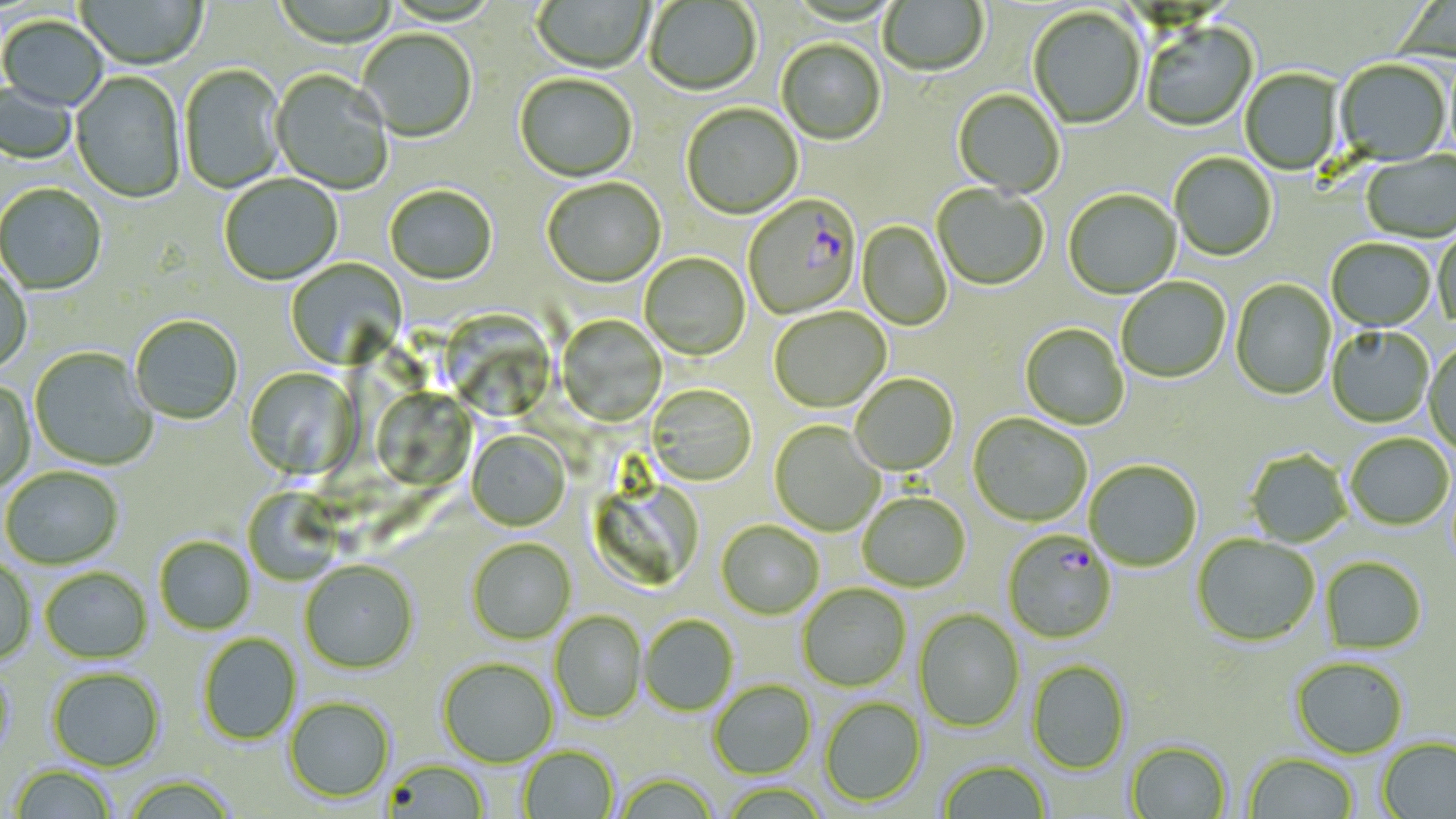

Summary:
  - Coordinate format: approximate bounding boxes as named x1/y1/x2/y2 corners in pixels
  - Uninfected red blood cell locations: (x1=272, y1=0, x2=399, y2=50), (x1=531, y1=0, x2=654, y2=75), (x1=879, y1=0, x2=988, y2=78), (x1=75, y1=1, x2=207, y2=72), (x1=644, y1=1, x2=761, y2=97), (x1=1028, y1=8, x2=1146, y2=130), (x1=0, y1=17, x2=108, y2=113), (x1=1141, y1=23, x2=1259, y2=133), (x1=356, y1=30, x2=477, y2=144), (x1=777, y1=41, x2=886, y2=146), (x1=1334, y1=61, x2=1451, y2=166), (x1=179, y1=65, x2=288, y2=195), (x1=1240, y1=69, x2=1344, y2=176), (x1=270, y1=71, x2=393, y2=195), (x1=70, y1=73, x2=186, y2=204), (x1=515, y1=76, x2=638, y2=183), (x1=0, y1=81, x2=77, y2=166), (x1=953, y1=90, x2=1065, y2=199), (x1=681, y1=104, x2=803, y2=220), (x1=1362, y1=152, x2=1456, y2=244), (x1=1169, y1=154, x2=1277, y2=262), (x1=220, y1=175, x2=343, y2=287), (x1=543, y1=179, x2=666, y2=290), (x1=0, y1=185, x2=107, y2=296), (x1=932, y1=185, x2=1049, y2=291), (x1=384, y1=187, x2=498, y2=287), (x1=1064, y1=190, x2=1181, y2=299), (x1=858, y1=221, x2=952, y2=332), (x1=1434, y1=229, x2=1456, y2=331), (x1=1326, y1=239, x2=1436, y2=333), (x1=639, y1=253, x2=751, y2=361), (x1=285, y1=257, x2=408, y2=370), (x1=0, y1=265, x2=32, y2=375), (x1=1116, y1=278, x2=1231, y2=383), (x1=1230, y1=279, x2=1336, y2=400), (x1=770, y1=308, x2=892, y2=413), (x1=436, y1=309, x2=559, y2=423), (x1=130, y1=315, x2=243, y2=425), (x1=557, y1=315, x2=666, y2=427), (x1=1020, y1=324, x2=1130, y2=430), (x1=1327, y1=327, x2=1434, y2=428), (x1=1424, y1=342, x2=1456, y2=455), (x1=30, y1=348, x2=157, y2=471), (x1=243, y1=367, x2=361, y2=481), (x1=851, y1=374, x2=959, y2=476), (x1=0, y1=379, x2=36, y2=492), (x1=646, y1=384, x2=757, y2=486), (x1=370, y1=388, x2=477, y2=491), (x1=969, y1=414, x2=1091, y2=527), (x1=769, y1=421, x2=884, y2=536), (x1=466, y1=431, x2=570, y2=532), (x1=1346, y1=434, x2=1454, y2=530), (x1=1245, y1=449, x2=1351, y2=547), (x1=1084, y1=460, x2=1202, y2=572), (x1=1, y1=467, x2=123, y2=569), (x1=243, y1=488, x2=344, y2=586), (x1=858, y1=493, x2=971, y2=592), (x1=716, y1=520, x2=824, y2=619), (x1=1192, y1=535, x2=1320, y2=647), (x1=155, y1=536, x2=255, y2=635), (x1=467, y1=538, x2=576, y2=644), (x1=1321, y1=557, x2=1426, y2=653), (x1=0, y1=559, x2=36, y2=664), (x1=299, y1=561, x2=418, y2=674), (x1=40, y1=567, x2=152, y2=663), (x1=797, y1=583, x2=911, y2=692), (x1=913, y1=609, x2=1024, y2=732), (x1=550, y1=610, x2=647, y2=723), (x1=640, y1=615, x2=738, y2=716), (x1=198, y1=633, x2=301, y2=745), (x1=437, y1=657, x2=558, y2=767), (x1=1291, y1=657, x2=1409, y2=758), (x1=1027, y1=659, x2=1131, y2=775), (x1=0, y1=662, x2=18, y2=762), (x1=47, y1=668, x2=165, y2=771), (x1=709, y1=680, x2=816, y2=779), (x1=284, y1=696, x2=395, y2=802), (x1=820, y1=697, x2=927, y2=807), (x1=1377, y1=737, x2=1456, y2=818), (x1=1124, y1=741, x2=1232, y2=818), (x1=518, y1=746, x2=619, y2=819), (x1=1243, y1=753, x2=1358, y2=818), (x1=381, y1=758, x2=490, y2=818), (x1=938, y1=760, x2=1051, y2=819), (x1=9, y1=765, x2=117, y2=818), (x1=614, y1=772, x2=719, y2=819), (x1=122, y1=775, x2=237, y2=819)
  - Plasmodium falciparum-infected red blood cell locations: (x1=743, y1=195, x2=862, y2=320), (x1=1002, y1=530, x2=1118, y2=643)
  - Slide-level diagnosis: Plasmodium falciparum
  - Preparation: thin blood smear
  - Image size: 1456×819 pixels
  - Modality: optical microscopy
  - Field of view: one of a larger specimen
  - Magnification: 1000x
  - Stain: May-Grünwald-Giemsa